Report the malaria status of this cell.
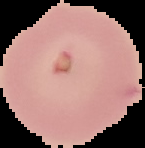

It is uninfected.

Summary:
  - Image type: segmented cell region with the area outside set to black
  - Preparation: thin blood film
  - Image size: 145×148 pixels